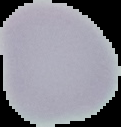

image size = 121×127 pixels
image type = segmented cell region on a black background
preparation = thin blood film
result = negative for Plasmodium parasites